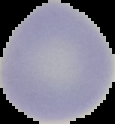

From a thin blood smear. Result: no Plasmodium parasites detected. Image is 115×124 pixels. Cell region segmented out of the field of view; the surrounding area is masked to black.